State which parasite is depicted.
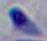

This is Toxoplasma gondii.

Summary:
  - Magnification: 1000x
  - Modality: micrograph